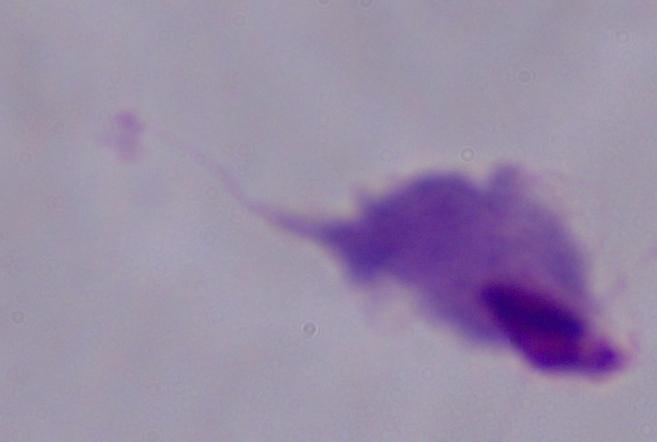

Summary:
  - Identification: trichomonad
  - Modality: micrograph
  - Magnification: 1000x